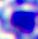
Photomicrograph. A leukocyte is shown. Captured at 400x magnification.